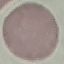
Summary:
  - Result: no malaria parasites seen
  - Stain: Giemsa
  - Image type: automatically extracted cell patch, resized to 64 × 64 pixels
  - Preparation: thin blood smear
  - Capture: smartphone through the microscope eyepiece